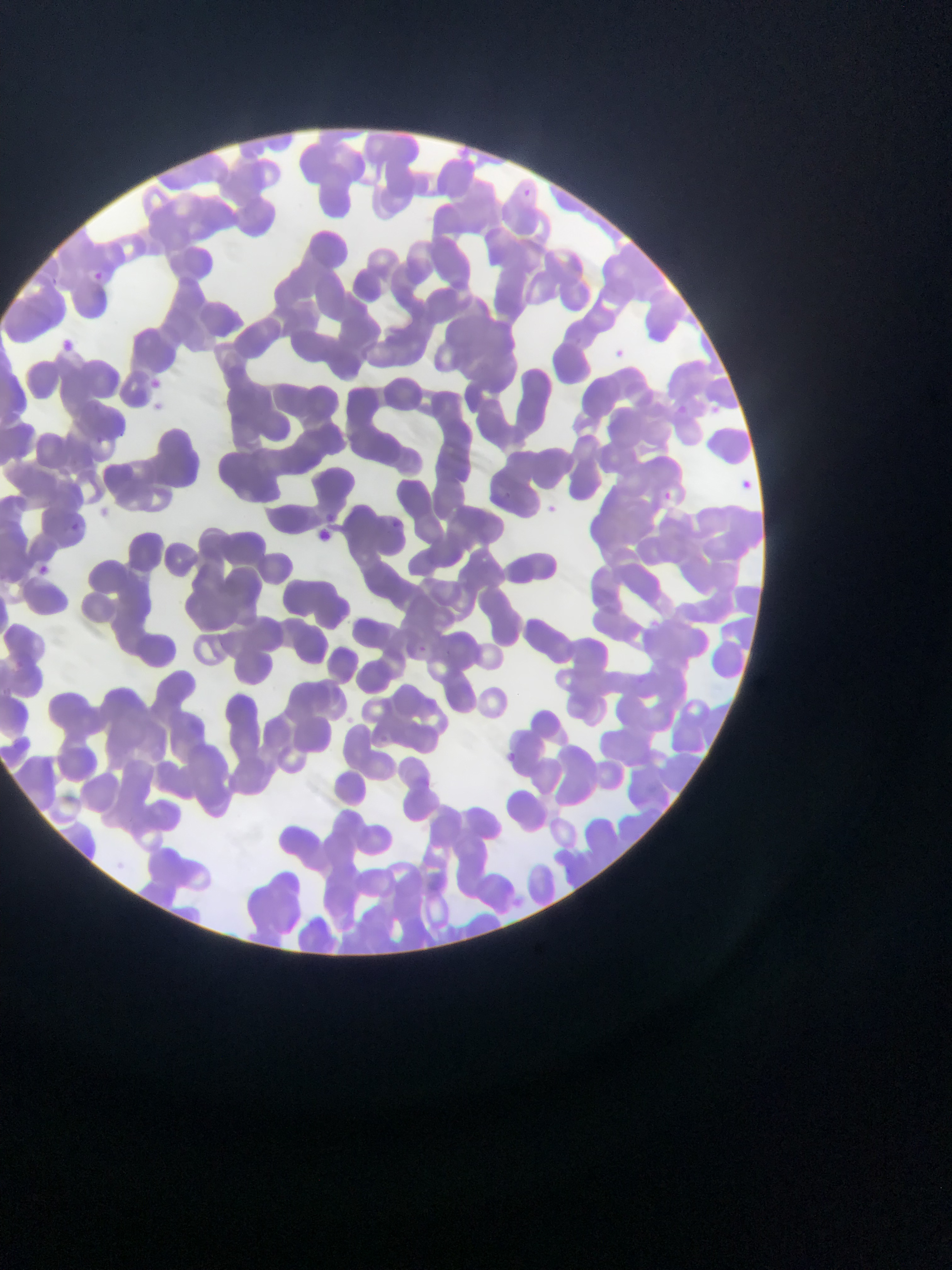

Approximate bounding boxes as {left, top, right, bottom} in pixels. Plasmodium parasite locations: {92, 265, 108, 286}, {53, 337, 90, 347}, {147, 371, 168, 388}, {147, 396, 163, 412}, {737, 473, 754, 496}, {662, 487, 671, 500}, {545, 500, 560, 517}, {319, 510, 339, 520}, {387, 514, 399, 528}, {68, 517, 86, 531}, {314, 527, 334, 543}, {35, 561, 52, 586}. Sample from Ghana. Thin blood smear. One field of view. Photographed through a microscope with a mobile-phone camera. Image is 952×1270 pixels.